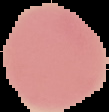

preparation: thin blood film
malaria_status: uninfected
image_size: 109×112 pixels
image_type: cell region segmented out of the field of view; surrounding area masked to black